Point out every malaria parasite and every leukocyte.
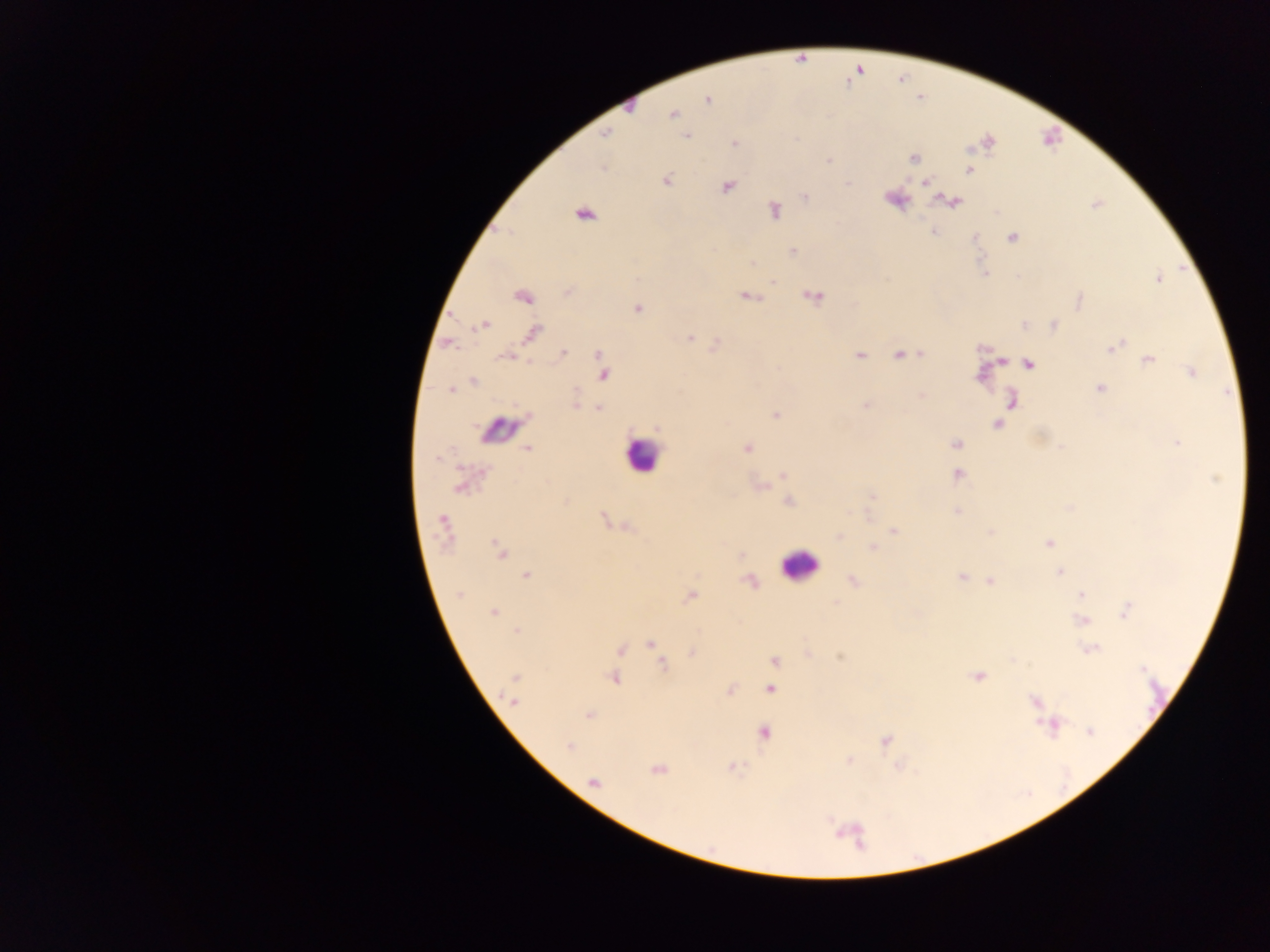

Approximate centers as x y in pixels.
Malaria parasites: 707 99; 628 106; 672 113; 604 135; 686 135; 735 143; 914 158; 829 161; 603 167; 969 169; 666 180; 925 182; 727 186; 805 196; 894 199; 953 201; 774 211; 583 213; 932 232; 1010 237; 792 250; 984 273; 1158 278; 568 291; 522 295; 813 295; 745 296; 1078 299; 637 309; 483 324; 1025 325; 1053 326; 532 333; 690 338; 447 343; 716 344; 1117 345; 919 352; 599 354; 860 354; 900 354; 508 355; 1148 360; 999 361; 1029 364; 555 372; 1192 372; 603 373; 473 382; 1099 388; 450 390; 922 394; 1011 401; 575 404; 866 406; 598 408; 775 415; 996 423; 1178 441; 956 445; 527 448; 747 448; 957 474; 783 475; 460 486; 760 486; 871 496; 788 500; 1069 507; 956 511; 604 519; 443 524; 626 527; 893 530; 990 533; 838 536; 1049 543; 873 547; 499 551; 1059 571; 526 575; 963 576; 749 581; 852 581; 989 581; 459 594; 689 595; 1081 595; 1126 610; 493 612; 1082 621; 517 631; 650 644; 620 649; 1090 649; 692 651; 660 657; 774 661; 663 665; 978 676; 613 677; 516 678; 770 688; 730 690; 512 701; 1034 702; 588 715; 1050 725; 1089 731; 763 732; 885 740; 569 746; 849 760; 732 767; 657 769; 593 781.
Leukocytes: 498 432; 641 454; 799 565.

preparation: thick blood film
country: Ghana
field_of_view: single
image_size: 1270×952 pixels
capture: mobile-phone photograph through a microscope